Assess the morphology of the erythrocytes.
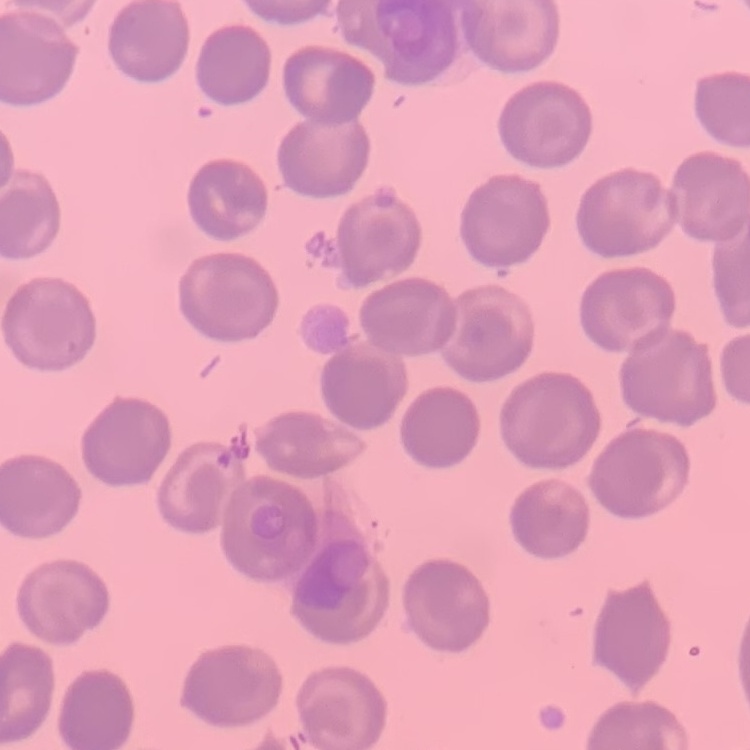

No rouleaux formation.

One tile cut from a larger photomicrograph. Field's or Giemsa stain. Thin blood smear.